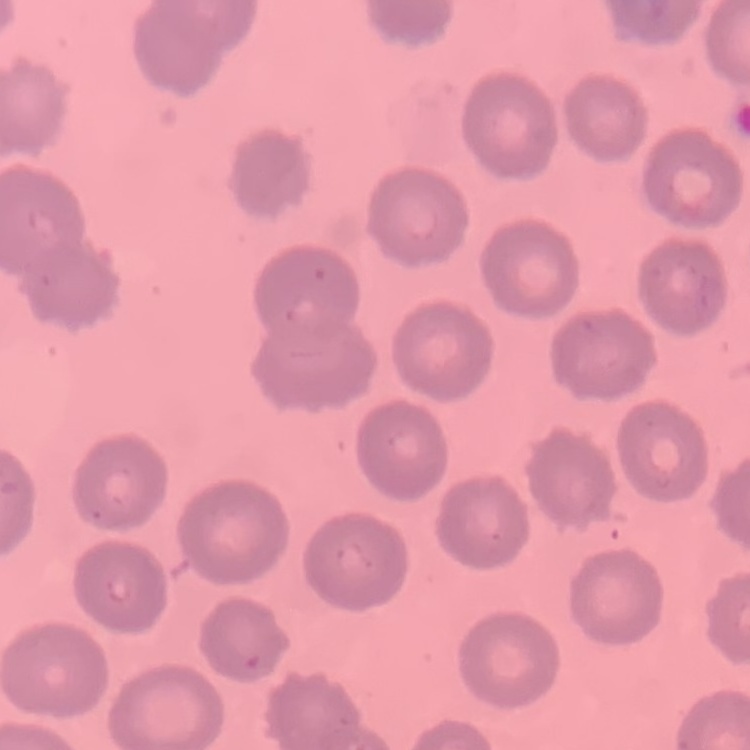

{
  "red_blood_cell_morphology": "no rouleaux formation",
  "stain": "Field's or Giemsa",
  "image_type": "one tile cut from a larger photomicrograph",
  "preparation": "thin blood film"
}